Classify this cell by malaria status.
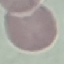
It is uninfected.

Summary:
  - Preparation: thin blood smear
  - Stain: Giemsa
  - Capture: smartphone through the microscope eyepiece
  - Image type: automatically extracted cell patch, resized to 64 × 64 pixels